Assess the morphology of the red blood cells.
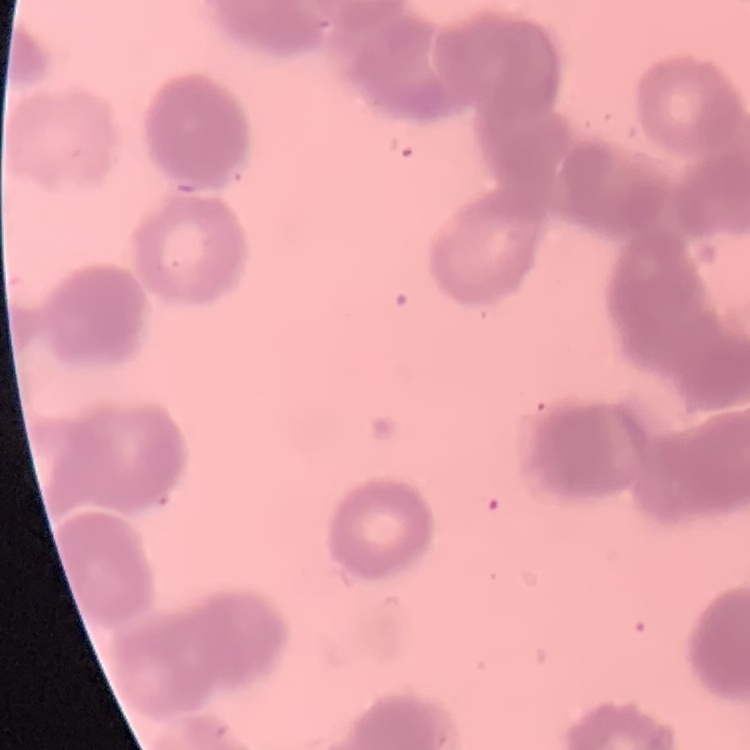

Rouleaux formation.

Thin blood smear. Field's or Giemsa stain. Square crop of a larger photomicrograph.